Locate every blood parasite and identify its species.
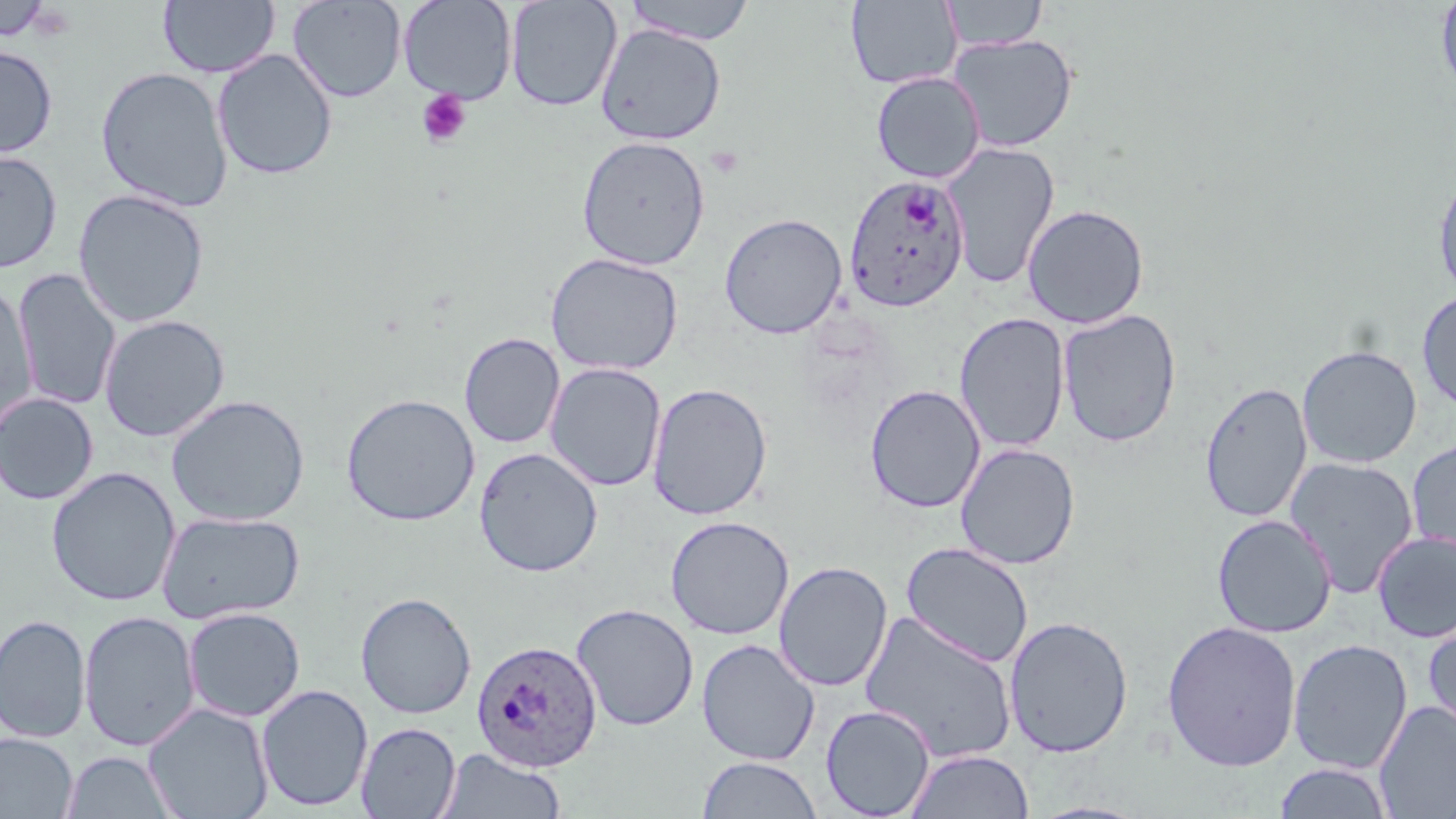

Approximate bounding boxes as named x1/y1/x2/y2 corners in pixels.
Plasmodium ovale-infected red blood cells: (x1=844, y1=175, x2=970, y2=313), (x1=472, y1=639, x2=602, y2=772).
No Plasmodium falciparum, Plasmodium malariae, Plasmodium vivax, Babesia divergens, or Trypanosoma brucei observed.

Summary:
  - Platelet locations: (x1=417, y1=88, x2=472, y2=148)
  - Uninfected red blood cell locations: (x1=287, y1=0, x2=406, y2=103), (x1=397, y1=0, x2=517, y2=104), (x1=505, y1=0, x2=622, y2=112), (x1=623, y1=0, x2=757, y2=45), (x1=1435, y1=0, x2=1456, y2=97), (x1=0, y1=1, x2=52, y2=41), (x1=158, y1=1, x2=280, y2=79), (x1=846, y1=1, x2=962, y2=89), (x1=940, y1=1, x2=1048, y2=51), (x1=595, y1=24, x2=727, y2=145), (x1=947, y1=33, x2=1079, y2=153), (x1=0, y1=45, x2=57, y2=159), (x1=212, y1=49, x2=338, y2=180), (x1=95, y1=66, x2=234, y2=212), (x1=871, y1=71, x2=985, y2=183), (x1=576, y1=135, x2=711, y2=270), (x1=942, y1=141, x2=1060, y2=289), (x1=0, y1=150, x2=62, y2=273), (x1=1432, y1=168, x2=1456, y2=302), (x1=72, y1=189, x2=210, y2=328), (x1=1022, y1=203, x2=1150, y2=329), (x1=719, y1=213, x2=847, y2=339), (x1=545, y1=252, x2=683, y2=376), (x1=12, y1=269, x2=121, y2=411), (x1=0, y1=284, x2=37, y2=433), (x1=1417, y1=291, x2=1456, y2=414), (x1=1057, y1=309, x2=1182, y2=447), (x1=954, y1=312, x2=1071, y2=453), (x1=99, y1=314, x2=230, y2=442), (x1=459, y1=332, x2=565, y2=449), (x1=1297, y1=345, x2=1422, y2=468), (x1=545, y1=362, x2=666, y2=492), (x1=1199, y1=381, x2=1312, y2=523), (x1=646, y1=382, x2=773, y2=520), (x1=865, y1=384, x2=985, y2=514), (x1=0, y1=393, x2=99, y2=505), (x1=341, y1=393, x2=480, y2=526), (x1=166, y1=394, x2=310, y2=526), (x1=1406, y1=437, x2=1456, y2=562), (x1=955, y1=442, x2=1080, y2=570), (x1=474, y1=446, x2=603, y2=577), (x1=1284, y1=456, x2=1419, y2=598), (x1=46, y1=466, x2=180, y2=607), (x1=156, y1=510, x2=305, y2=624), (x1=1211, y1=514, x2=1337, y2=638), (x1=665, y1=515, x2=794, y2=640), (x1=1372, y1=531, x2=1456, y2=643), (x1=900, y1=542, x2=1034, y2=667), (x1=773, y1=561, x2=892, y2=692), (x1=355, y1=591, x2=476, y2=720), (x1=571, y1=603, x2=699, y2=731), (x1=182, y1=607, x2=305, y2=722), (x1=79, y1=610, x2=200, y2=751), (x1=859, y1=610, x2=1019, y2=764), (x1=0, y1=614, x2=91, y2=743), (x1=1422, y1=614, x2=1456, y2=745), (x1=1003, y1=615, x2=1134, y2=758), (x1=1161, y1=620, x2=1302, y2=771), (x1=696, y1=638, x2=820, y2=766), (x1=1287, y1=639, x2=1413, y2=774), (x1=256, y1=683, x2=373, y2=812), (x1=1374, y1=701, x2=1456, y2=819), (x1=143, y1=702, x2=274, y2=819), (x1=820, y1=704, x2=936, y2=818), (x1=356, y1=721, x2=461, y2=818), (x1=0, y1=733, x2=77, y2=818), (x1=435, y1=748, x2=566, y2=819), (x1=905, y1=748, x2=1034, y2=819), (x1=61, y1=751, x2=178, y2=818), (x1=697, y1=756, x2=821, y2=818), (x1=1273, y1=763, x2=1395, y2=819)
  - Slide-level diagnosis: Plasmodium ovale
  - Image size: 1456×819 pixels
  - Modality: optical microscopy
  - Stain: May-Grünwald-Giemsa
  - Preparation: thin blood film
  - Field of view: single
  - Magnification: 1000x